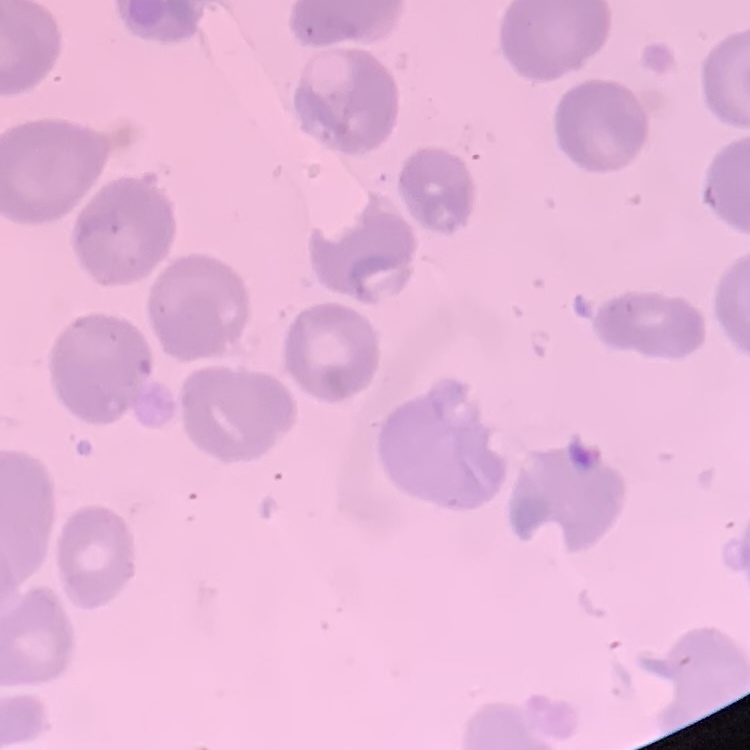 The erythrocytes exhibit no rouleaux formation. Thin peripheral smear. Stained with either Field's or Giemsa. One tile cut from a larger photomicrograph.